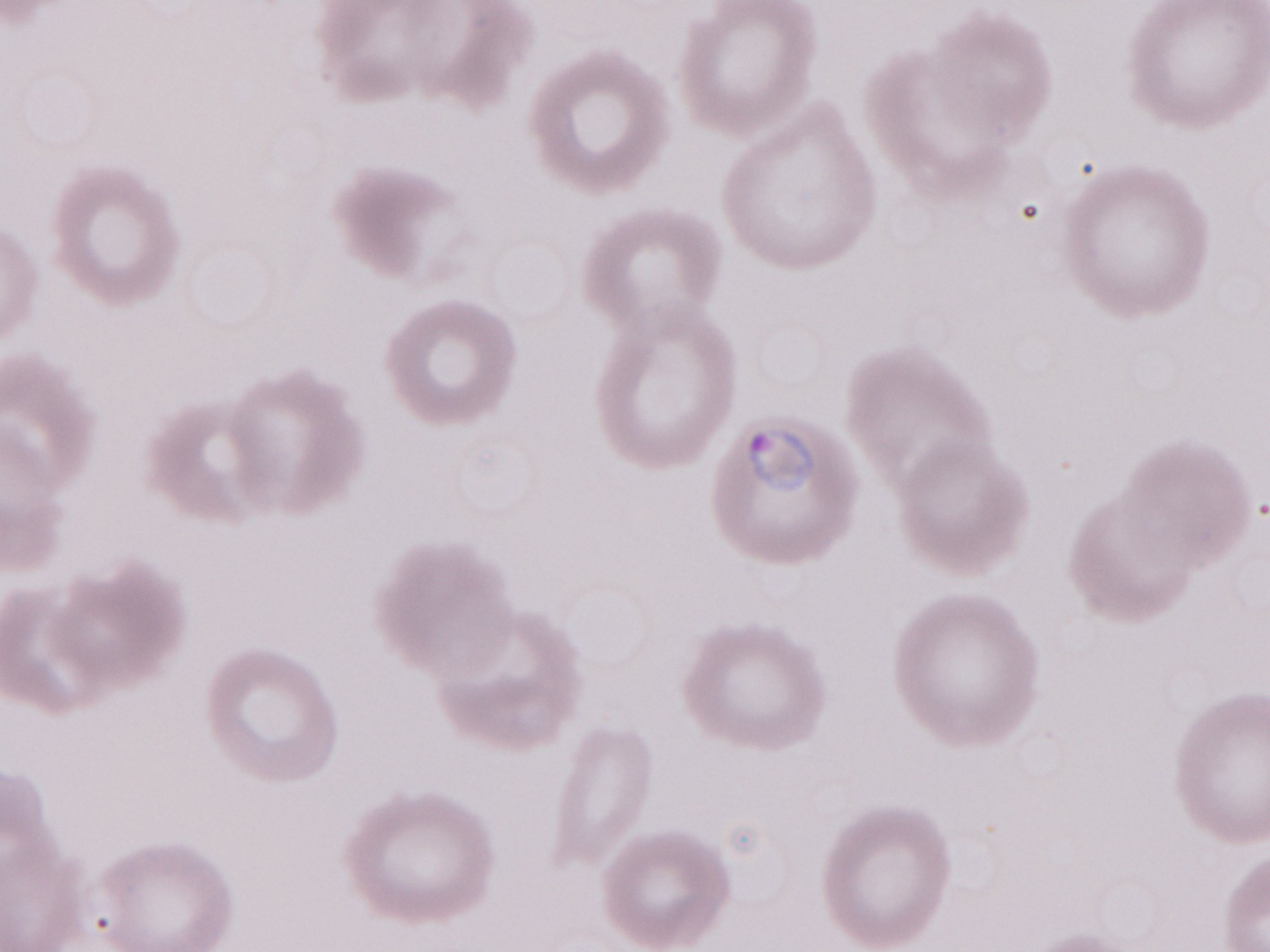
Olympus BX43 microscope and DP73 digital camera. Patient-level malaria diagnosis: positive. Thin blood film. Single field of view. May-Grünwald-Giemsa (MGG) stain. Image is 1270×952 pixels. 1,000x magnification.